Assess this cell for malaria.
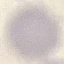

It is uninfected.

preparation = thin blood smear
stain = Giemsa
image type = cell patch, automatically extracted from a larger field of view and resized to 64 × 64 pixels
capture = smartphone through the microscope eyepiece